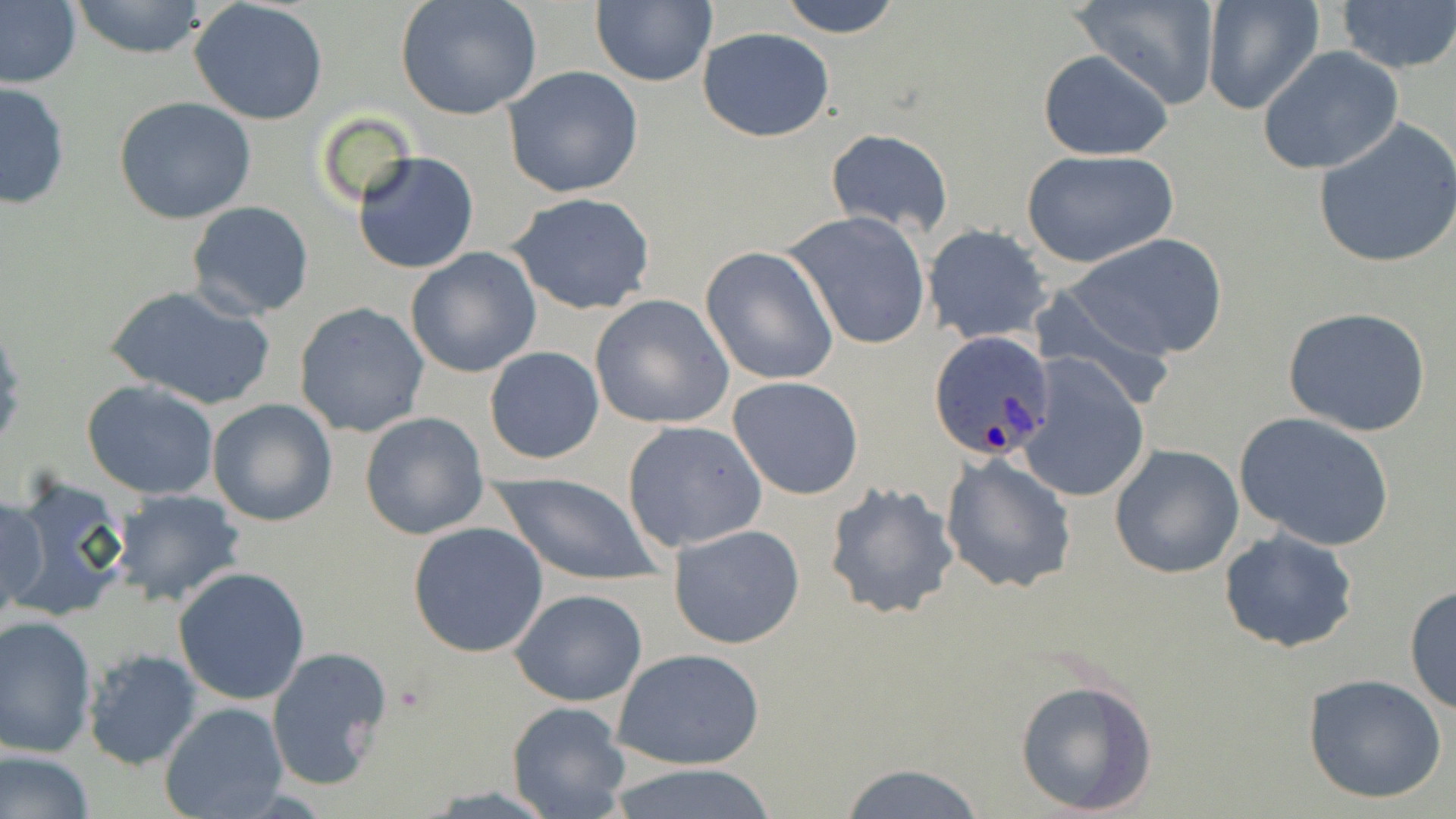

slide-level diagnosis = Plasmodium ovale
image size = 1456×819 pixels
Plasmodium ovale-infected red blood cell locations = approximate bounding boxes as (x1,y1)-(x2,y2) corner pairs in pixels: (927,331)-(1057,465)
modality = optical microscopy
preparation = thin blood film
uninfected red blood cell locations = approximate bounding boxes as (x1,y1)-(x2,y2) corner pairs in pixels: (0,0)-(82,90), (395,0)-(543,122), (589,0)-(716,88), (776,0)-(905,38), (1070,0)-(1221,107), (67,1)-(212,59), (1201,1)-(1323,115), (1336,1)-(1456,74), (189,2)-(330,125), (698,26)-(835,142), (1258,48)-(1404,176), (1037,50)-(1173,161), (501,66)-(644,197), (0,80)-(72,210), (112,96)-(260,224), (1312,119)-(1456,267), (826,129)-(953,237), (1019,149)-(1179,269), (352,150)-(480,275), (506,191)-(659,317), (184,200)-(314,321), (785,211)-(930,349), (924,225)-(1053,344), (1066,234)-(1228,360), (700,246)-(839,386), (405,248)-(543,378), (1028,283)-(1177,408), (104,284)-(275,411), (589,294)-(736,430), (293,301)-(432,438), (1282,307)-(1432,437), (483,345)-(604,465), (1019,358)-(1151,505), (727,376)-(865,500), (82,381)-(222,499), (208,399)-(337,527), (1233,411)-(1396,551), (359,412)-(490,541), (621,420)-(768,552), (1108,444)-(1244,579), (940,453)-(1078,594), (493,472)-(659,587), (4,473)-(132,622), (822,480)-(962,620), (107,488)-(247,608), (1,492)-(46,624), (407,520)-(549,658), (669,523)-(806,648), (1219,528)-(1359,654), (173,567)-(310,706), (1404,584)-(1455,716), (510,588)-(648,708), (1,615)-(99,756), (264,645)-(393,793), (611,646)-(768,772), (81,649)-(203,770), (1301,674)-(1448,806), (1014,677)-(1160,816), (506,701)-(632,818), (159,702)-(290,819), (0,749)-(96,819), (833,760)-(992,819), (605,766)-(784,819)
stain = May-Grünwald-Giemsa
field of view = one of a larger specimen
magnification = 1000x